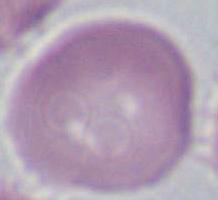

A red blood cell is shown. Captured at 1000x magnification. Photomicrograph.